State which parasite is depicted.
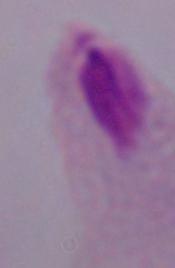

This is a trichomonad.

Summary:
  - Magnification: 1000x
  - Modality: micrograph